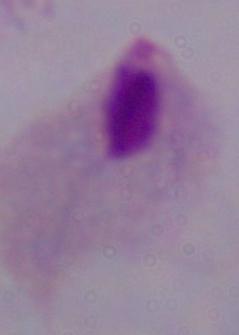
{
  "identification": "trichomonad",
  "magnification": "1000x",
  "modality": "photomicrograph"
}